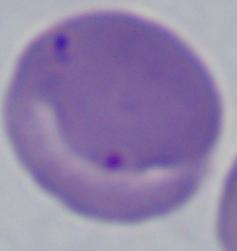
Summary:
  - Modality: photomicrograph
  - Identification: Babesia
  - Magnification: 1000x